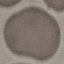

Summary:
  - Result: no malaria parasites seen
  - Capture: smartphone through the microscope eyepiece
  - Image type: automatically extracted cell patch, resized to 64 × 64 pixels
  - Stain: Giemsa
  - Preparation: thin blood film